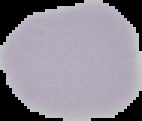
Image is 142×121 pixels. Malaria status: uninfected. Segmented cell region on a black background. From a thin blood film.